Assess the morphology of the red blood cells.
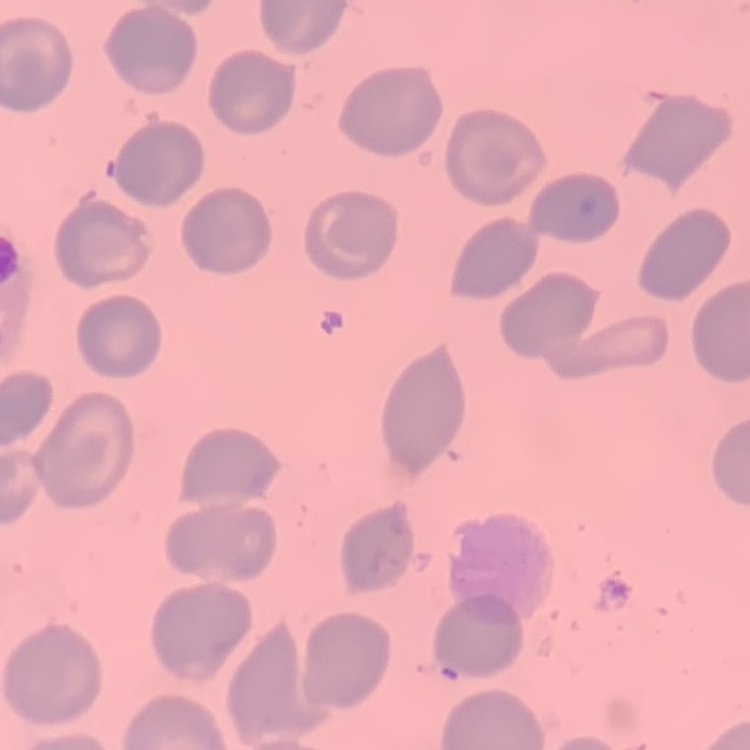

No rouleaux formation.

Summary:
  - Preparation: thin peripheral smear
  - Image type: one tile cut from a larger photomicrograph
  - Stain: Field's or Giemsa